Locate every Plasmodium falciparum-infected red blood cell.
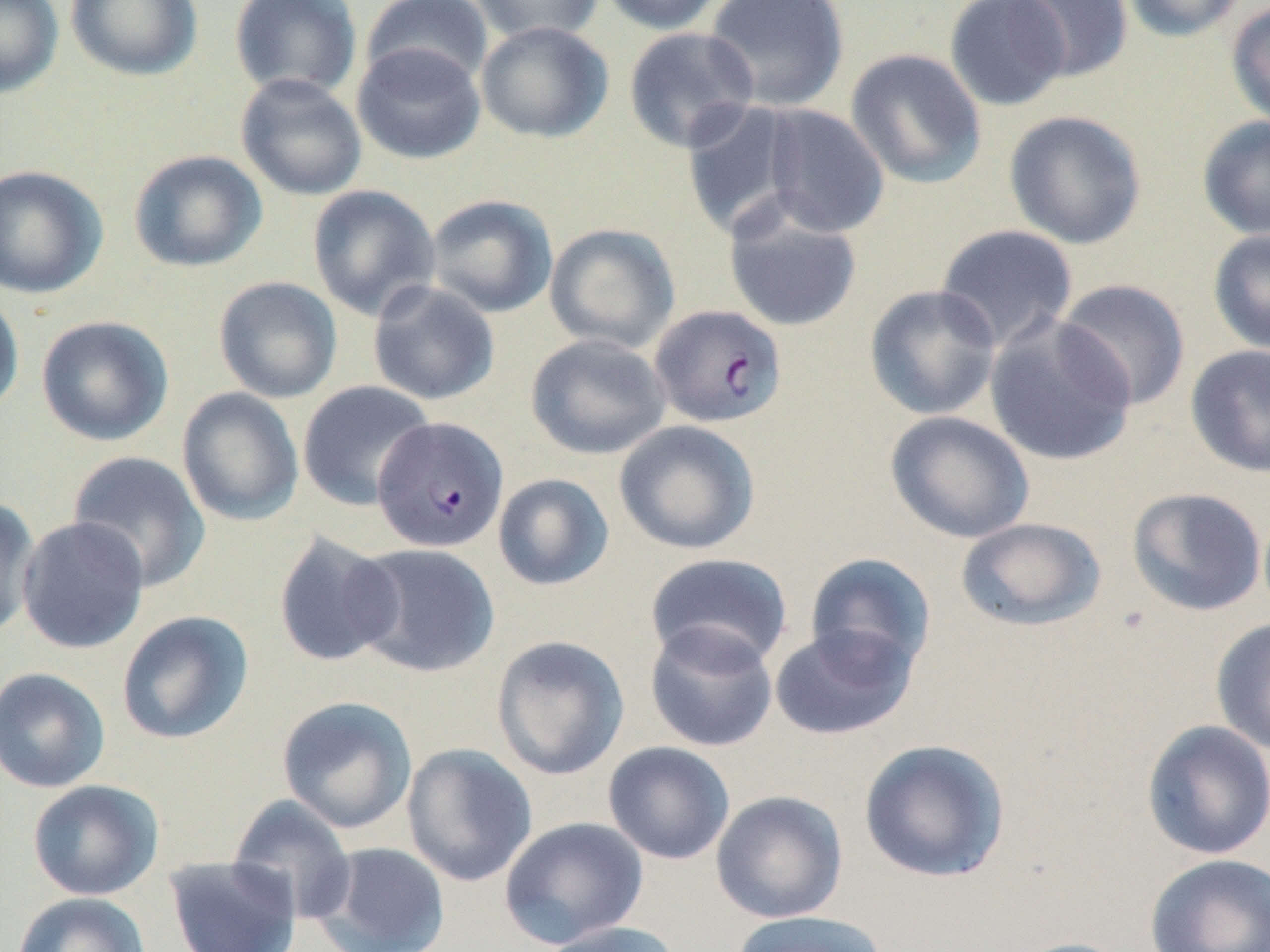
Approximate bounding boxes as [x1, y1, x2, y2] in pixels.
Plasmodium falciparum-infected red blood cells: [649, 304, 788, 428], [373, 416, 508, 553].

Uninfected red blood cell locations: [0, 0, 63, 98], [66, 0, 202, 81], [229, 0, 363, 101], [361, 0, 494, 90], [468, 0, 604, 46], [597, 0, 729, 35], [704, 0, 850, 112], [943, 0, 1071, 111], [1007, 0, 1134, 83], [1120, 0, 1249, 42], [1225, 1, 1270, 129], [475, 21, 614, 143], [623, 26, 760, 153], [351, 41, 486, 164], [845, 48, 987, 190], [235, 73, 368, 201], [679, 100, 809, 240], [759, 104, 890, 238], [1003, 110, 1147, 250], [1197, 114, 1270, 241], [128, 149, 267, 273], [0, 165, 108, 298], [307, 185, 440, 321], [425, 194, 558, 319], [722, 197, 863, 333], [544, 223, 680, 354], [935, 223, 1078, 352], [1207, 228, 1270, 356], [213, 275, 343, 403], [1055, 278, 1192, 411], [367, 280, 500, 406], [864, 284, 1001, 420], [0, 288, 25, 418], [984, 314, 1137, 467], [35, 315, 173, 447], [525, 334, 671, 460], [1185, 344, 1270, 478], [297, 380, 435, 511], [176, 387, 304, 526], [885, 411, 1035, 544], [614, 420, 761, 555], [67, 451, 211, 592], [493, 473, 614, 591], [1126, 487, 1267, 617], [0, 496, 41, 640], [16, 515, 149, 654], [956, 517, 1106, 632], [272, 530, 404, 668], [350, 543, 500, 678], [645, 552, 793, 671], [804, 552, 936, 677], [116, 610, 254, 745], [1210, 616, 1270, 755], [645, 622, 779, 752], [768, 623, 918, 741], [490, 634, 630, 781], [0, 666, 111, 793], [276, 695, 418, 833], [1141, 720, 1270, 861], [858, 738, 1010, 883], [603, 741, 736, 865], [401, 743, 538, 886], [27, 779, 163, 900], [711, 790, 848, 923], [227, 794, 358, 923], [498, 815, 650, 950], [311, 841, 451, 952], [1144, 853, 1270, 952], [164, 855, 302, 952], [12, 892, 151, 952], [729, 909, 892, 952], [536, 920, 685, 952], [1010, 936, 1137, 952]. Slide-level diagnosis: Plasmodium falciparum. One field of a larger specimen. Light microscopy. Image is 1270×952 pixels. May-Grünwald-Giemsa stain. 1000x magnification. Thin blood smear.